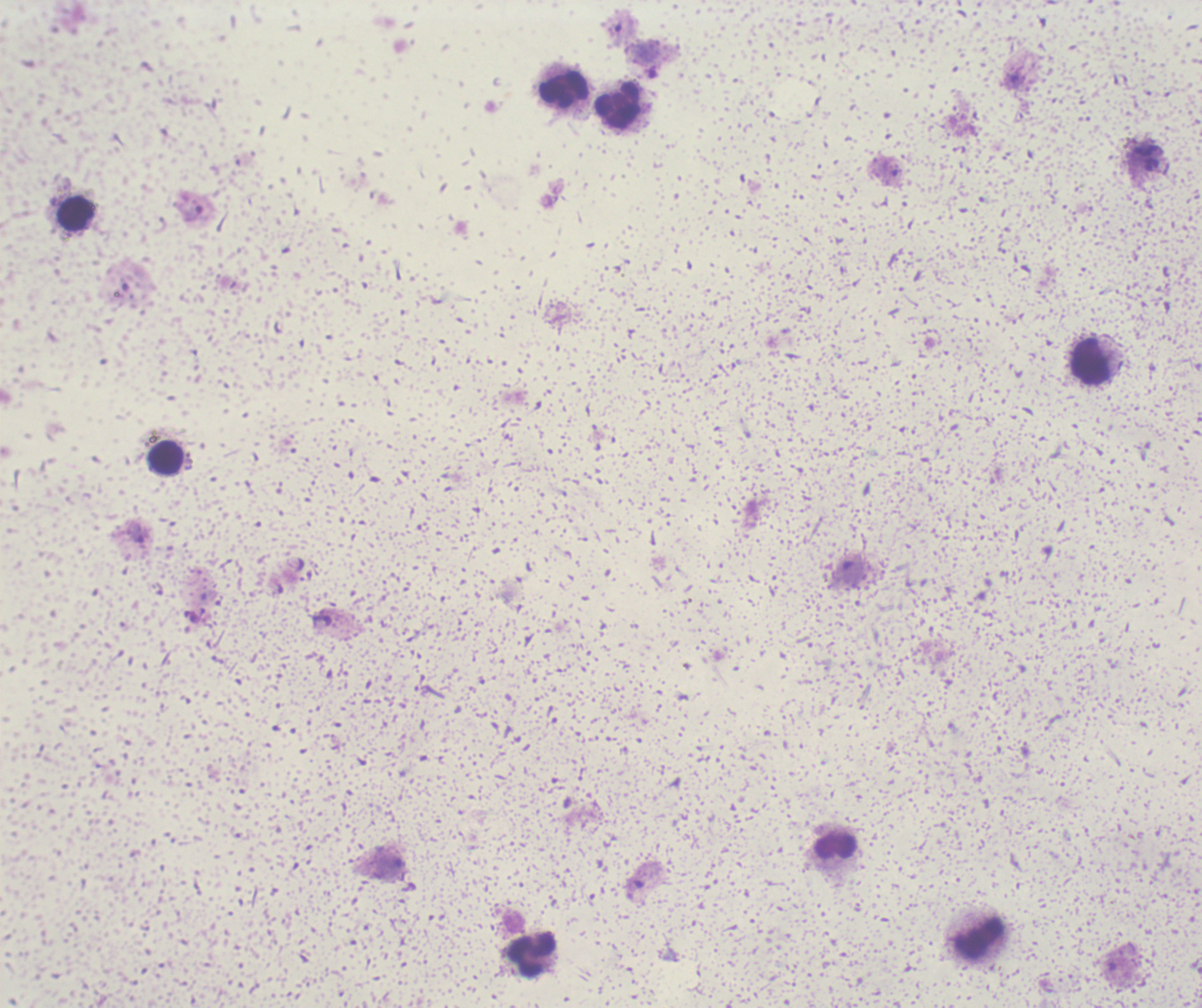
coordinate format = approximate centers as [x, y] in pixels
trophozoite locations = [137, 533]
leukocyte locations = [563, 90], [619, 106], [75, 215], [1091, 362], [167, 459], [836, 846], [532, 958]
field of view = one from this slide
result = Plasmodium parasites identified
stain = Romanowsky
preparation = thick blood smear
context = previously used in a real diagnosis
image size = 1202×1008 pixels
background quality = unsatisfactory
magnification = 100x